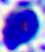
Summary:
  - Identification: white blood cell
  - Magnification: 400x
  - Modality: photomicrograph